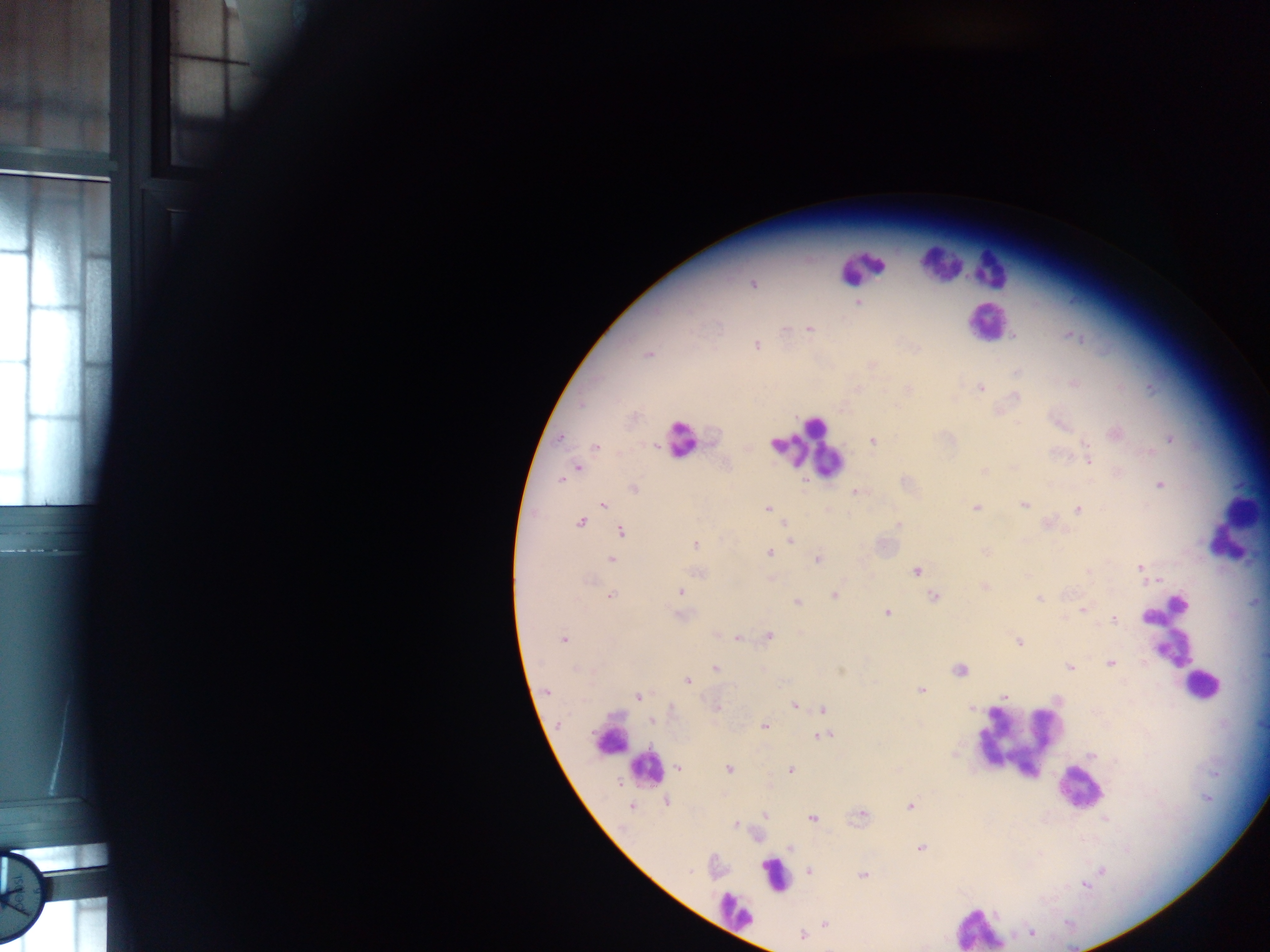

Approximate centers as [x, y] in pixels.
Summary:
  - Leukocyte locations: [942, 263], [967, 265], [861, 268], [992, 268], [985, 321], [680, 439], [808, 447], [1234, 529], [1169, 632], [1201, 686], [611, 735], [1018, 735], [1040, 756], [646, 769], [1078, 788], [775, 876], [735, 911], [979, 926]
  - Plasmodium parasite locations: [228, 13], [753, 283], [858, 303], [808, 329], [783, 330], [1070, 334], [1013, 337], [756, 345], [647, 353], [870, 364], [1017, 372], [1074, 384], [979, 387], [1120, 387], [1150, 387], [857, 388], [908, 389], [1114, 432], [1170, 438], [872, 440], [1084, 441], [596, 447], [1149, 452], [1089, 461], [577, 468], [984, 471], [1116, 472], [560, 479], [904, 482], [1159, 484], [632, 487], [856, 490], [1024, 504], [602, 505], [976, 507], [767, 509], [1077, 509], [828, 510], [580, 521], [898, 525], [1064, 530], [621, 532], [791, 541], [694, 544], [985, 551], [770, 553], [817, 558], [611, 560], [1139, 566], [916, 571], [698, 573], [771, 579], [984, 585], [679, 591], [610, 595], [835, 595], [934, 596], [1038, 598], [796, 602], [1256, 602], [1082, 609], [886, 613], [679, 615], [1114, 618], [717, 634], [769, 636], [738, 637], [563, 639], [1019, 641], [1110, 662], [1069, 667], [715, 668], [959, 669], [687, 680], [921, 690], [546, 691], [638, 696], [1005, 696], [794, 704], [715, 707], [971, 708], [822, 709], [652, 720], [764, 726], [822, 736], [679, 768], [728, 769], [790, 770], [666, 801], [630, 805], [909, 806], [765, 814], [860, 815], [812, 818], [1105, 819], [735, 824], [789, 847], [920, 848], [808, 870], [862, 875], [1083, 883], [824, 924], [1031, 932], [803, 935]
  - Field of view: single
  - Preparation: thick blood smear
  - Capture: mobile-phone photograph through a microscope
  - Image size: 1270×952 pixels
  - Country: Ghana